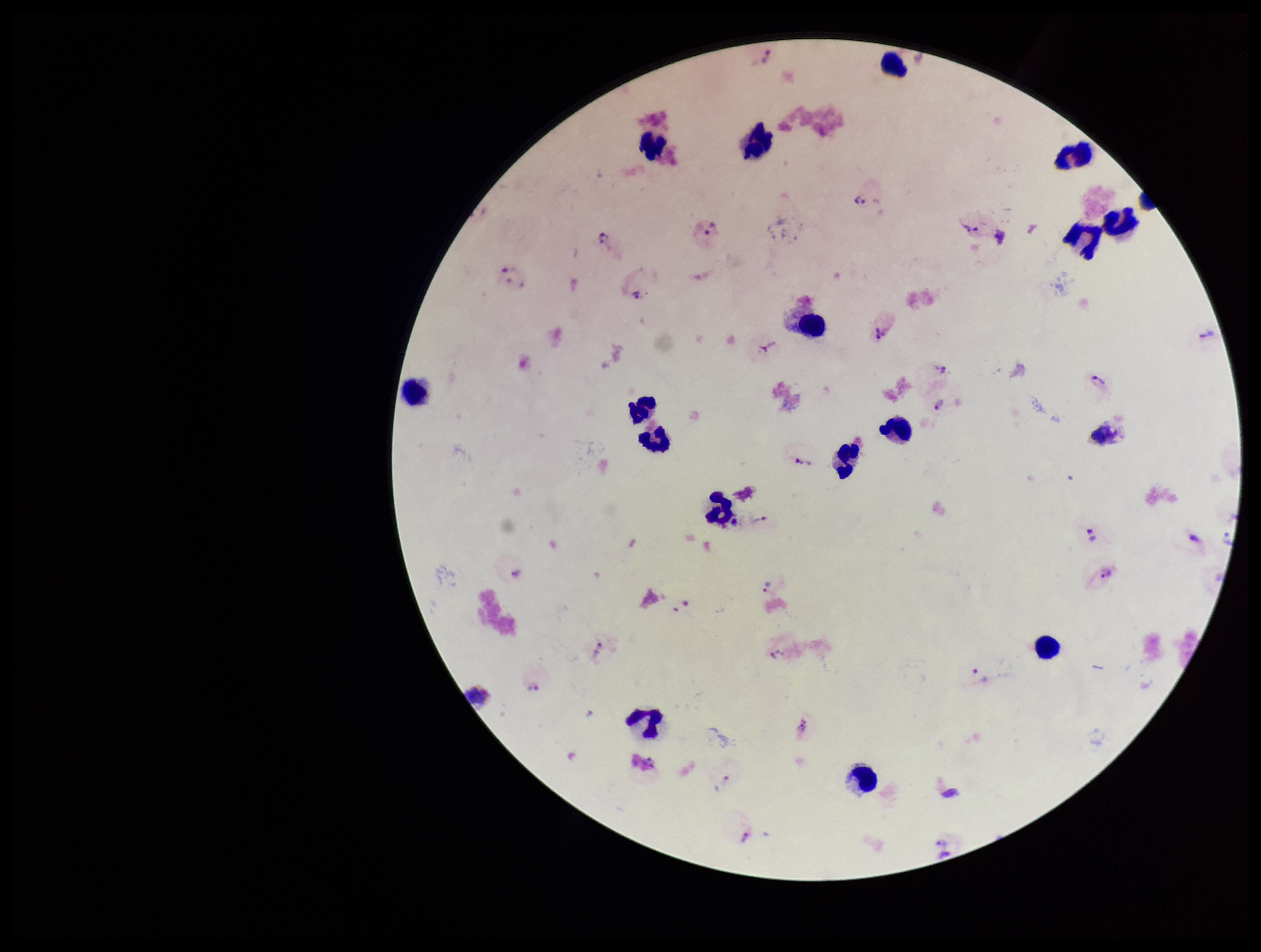
{
  "leukocyte_count": 18,
  "image_size": "1261×952 pixels",
  "stain": "Giemsa",
  "plasmodium_parasites": "seen",
  "parasite_count": 33,
  "preparation": "thick blood smear",
  "species_reported_for_this_patient": "Plasmodium vivax",
  "field_of_view": "single",
  "capture": "smartphone photograph through the microscope eyepiece",
  "patient_malaria_status": "positive"
}